State the blood parasite species.
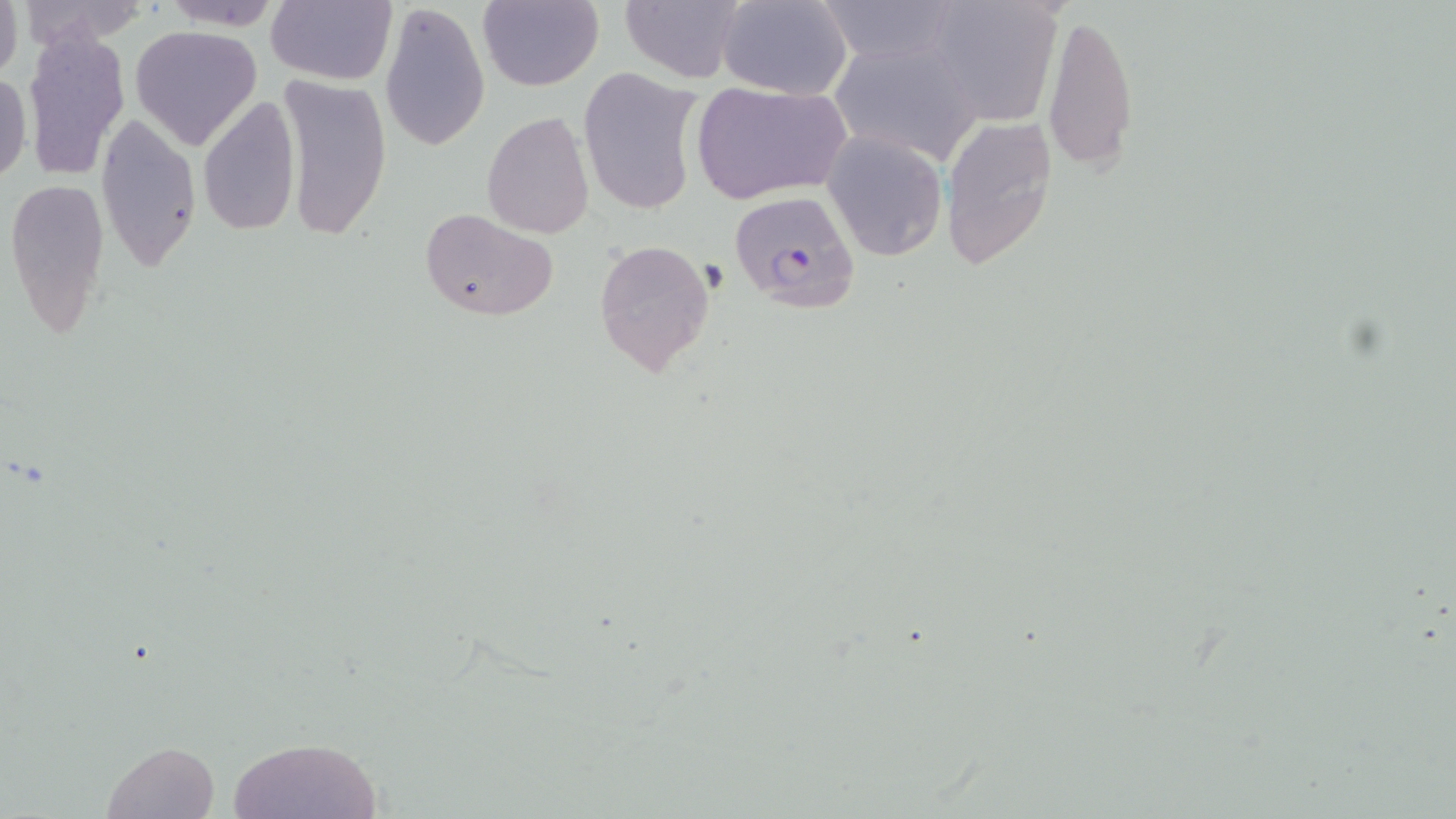

Plasmodium falciparum.

stain: May-Grünwald-Giemsa
preparation: thin blood film
magnification: 1000x
image_size: 1456×819 pixels
uninfected_red_blood_cell_locations: 'approximate bounding boxes as (x1, y1, x2, y2) in pixels: (0, 0, 23, 81), (13, 0, 156, 48), (160, 0, 281, 29), (268, 0, 397, 86), (478, 0, 604, 92), (619, 0, 744, 84), (718, 0, 852, 99), (822, 0, 965, 64), (921, 0, 1067, 125), (379, 1, 488, 153), (1041, 10, 1138, 173), (130, 24, 260, 147), (22, 28, 132, 183), (825, 36, 986, 168), (578, 67, 706, 219), (0, 72, 31, 183), (278, 74, 390, 242), (690, 81, 849, 203), (196, 95, 301, 237), (482, 111, 595, 240), (96, 112, 202, 269), (941, 114, 1058, 271), (823, 130, 948, 261), (6, 174, 110, 338), (419, 207, 556, 320), (592, 237, 714, 379), (226, 735, 384, 817), (100, 740, 219, 819)'
modality: light microscopy
plasmodium_falciparum_infected_red_blood_cell_locations: 'approximate bounding boxes as (x1, y1, x2, y2) in pixels: (727, 190, 861, 311)'
field_of_view: single